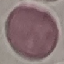 Malaria status: uninfected. Automatically extracted cell patch, resized to 64 × 64 pixels. Photographed with a smartphone camera at the microscope eyepiece. Thin smear of blood. Giemsa-stained preparation.